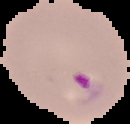

preparation = thin blood smear
image type = segmented cell region with the area outside set to black
result = Plasmodium parasites detected
image size = 130×124 pixels